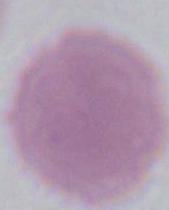
A red blood cell is seen. Captured at 1000x magnification. Micrograph.